Point out each Plasmodium parasite.
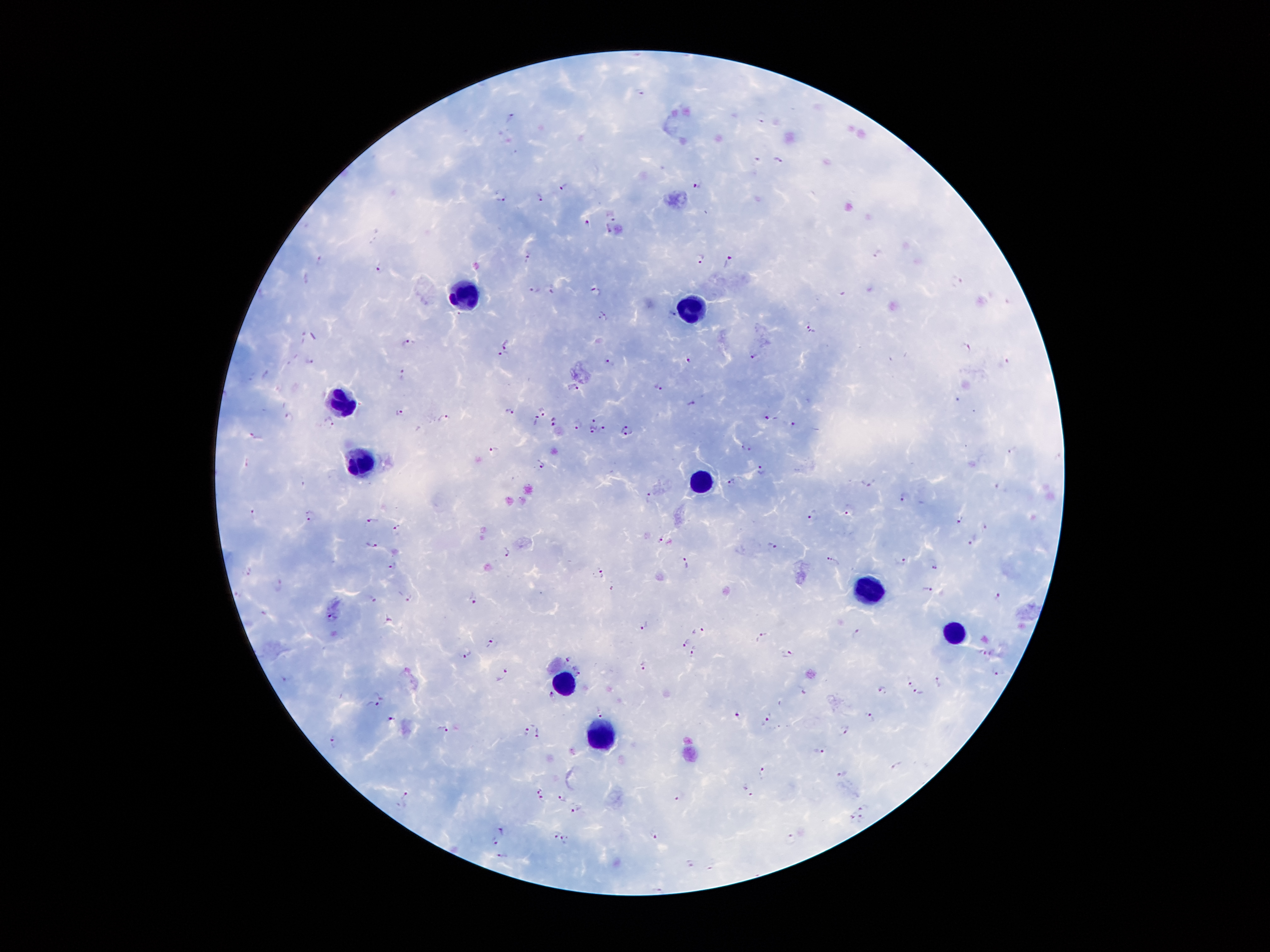
Approximate centers as {x, y} in pixels.
Plasmodium parasites: {640, 92}, {510, 118}, {761, 118}, {779, 160}, {700, 183}, {566, 184}, {500, 194}, {539, 197}, {587, 222}, {878, 254}, {527, 256}, {701, 257}, {321, 260}, {731, 263}, {379, 266}, {958, 282}, {549, 289}, {535, 290}, {596, 290}, {670, 314}, {604, 316}, {811, 327}, {303, 338}, {504, 342}, {409, 345}, {965, 347}, {500, 354}, {755, 355}, {687, 358}, {612, 361}, {309, 363}, {1006, 364}, {403, 373}, {251, 374}, {267, 374}, {658, 385}, {576, 387}, {692, 402}, {544, 407}, {512, 411}, {400, 412}, {289, 417}, {769, 417}, {443, 418}, {593, 418}, {555, 421}, {795, 421}, {330, 422}, {537, 422}, {576, 424}, {605, 428}, {593, 430}, {628, 431}, {256, 436}, {745, 449}, {493, 451}, {1014, 451}, {539, 466}, {759, 471}, {731, 483}, {868, 483}, {1003, 488}, {649, 497}, {903, 498}, {847, 511}, {254, 513}, {310, 515}, {813, 516}, {961, 520}, {371, 521}, {984, 527}, {398, 530}, {662, 540}, {973, 543}, {372, 544}, {769, 545}, {508, 553}, {904, 558}, {832, 561}, {685, 562}, {394, 565}, {934, 565}, {250, 568}, {601, 573}, {282, 585}, {613, 588}, {927, 590}, {998, 594}, {408, 598}, {372, 600}, {472, 600}, {331, 616}, {388, 620}, {644, 625}, {698, 630}, {857, 632}, {762, 636}, {685, 641}, {494, 644}, {694, 651}, {467, 653}, {787, 653}, {984, 654}, {568, 660}, {644, 667}, {578, 672}, {997, 672}, {505, 676}, {909, 681}, {940, 681}, {803, 691}, {882, 691}, {379, 693}, {550, 694}, {919, 694}, {374, 705}, {599, 713}, {871, 715}, {392, 718}, {768, 719}, {444, 730}, {526, 730}, {845, 731}, {539, 735}, {335, 741}, {816, 753}, {895, 765}, {763, 771}, {843, 774}, {537, 788}, {748, 788}, {406, 797}, {562, 797}, {680, 797}, {542, 800}, {865, 807}, {575, 808}, {850, 815}, {861, 820}, {502, 829}, {556, 832}, {655, 835}, {494, 840}, {565, 840}, {793, 842}, {502, 855}, {692, 862}, {711, 867}, {658, 889}.

leukocyte locations = {462, 294}, {688, 299}, {340, 403}, {357, 462}, {703, 483}, {867, 589}, {955, 629}, {567, 677}, {598, 735}
field of view = single
preparation = thick blood film
patient malaria status = positive for Plasmodium falciparum
capture = smartphone through the microscope eyepiece
image size = 1270×952 pixels
stain = Giemsa
magnification = 100x